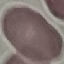
Result: negative for malaria parasites. Giemsa stain. Thin smear of blood. Cell patch, automatically extracted from a larger field of view and resized to 64 × 64 pixels. Photographed with a smartphone camera at the microscope eyepiece.